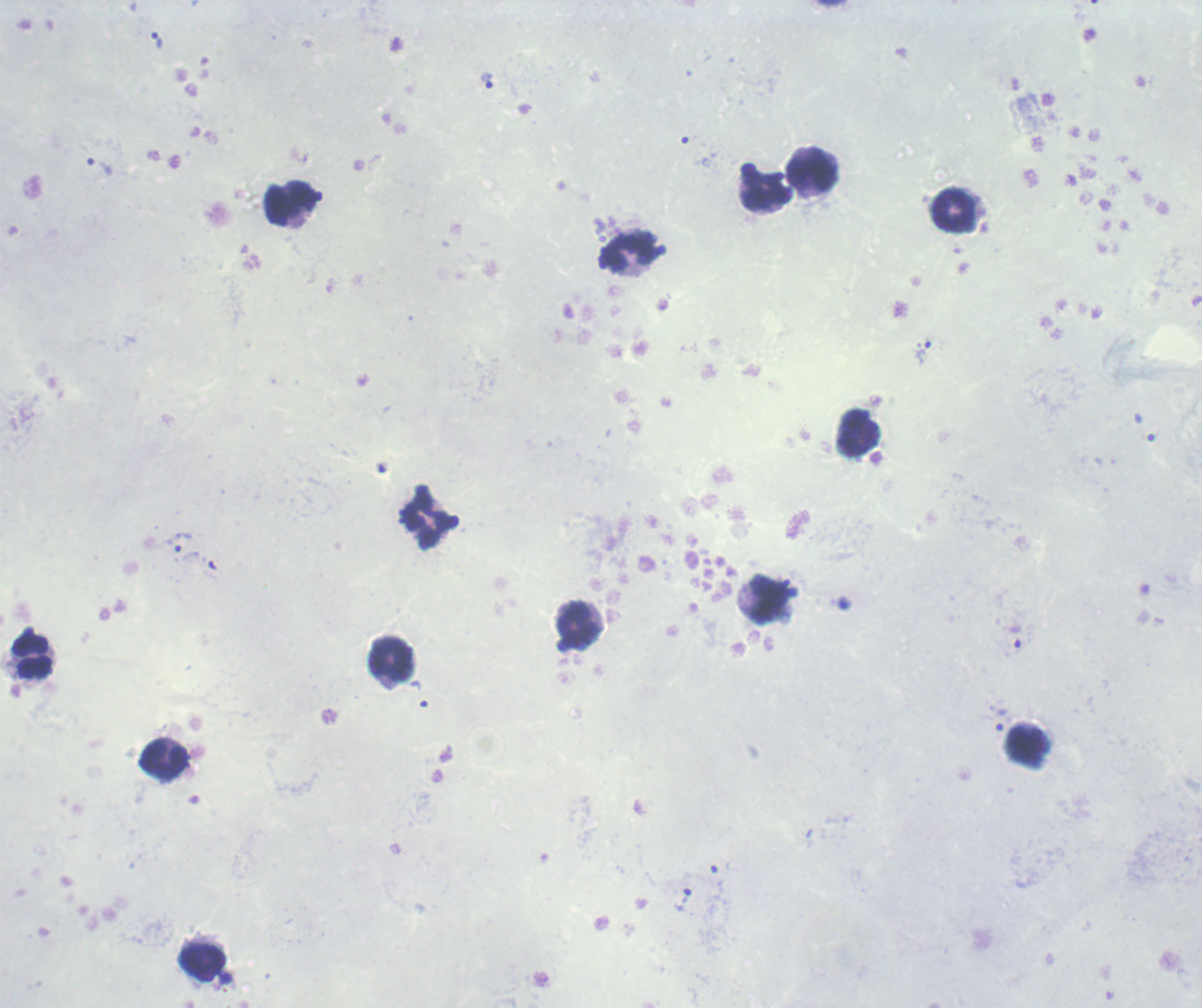

{
  "magnification": "100x",
  "background_quality": "poor",
  "preparation": "thick smear of blood",
  "field_of_view": "one from this slide",
  "trophozoite_locations": "approximate centers as [x, y] in pixels: [158, 41], [486, 81], [923, 353], [179, 542], [1015, 636], [1001, 720], [685, 896]",
  "image_size": "1202×1008 pixels",
  "leukocyte_locations": "approximate centers as [x, y] in pixels: [812, 169], [291, 202], [954, 210], [630, 252], [859, 433], [427, 522], [768, 600], [577, 625], [31, 655], [390, 658], [1027, 748], [164, 761], [201, 960]",
  "result": "malaria parasites identified",
  "stain": "Romanowsky",
  "context": "previously used in an actual diagnosis"
}